State which cell type is depicted.
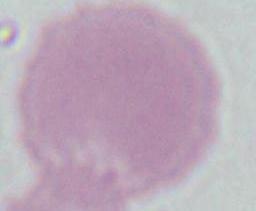
This is an erythrocyte.

Captured at 1000x magnification. Micrograph.